Evaluate for malaria.
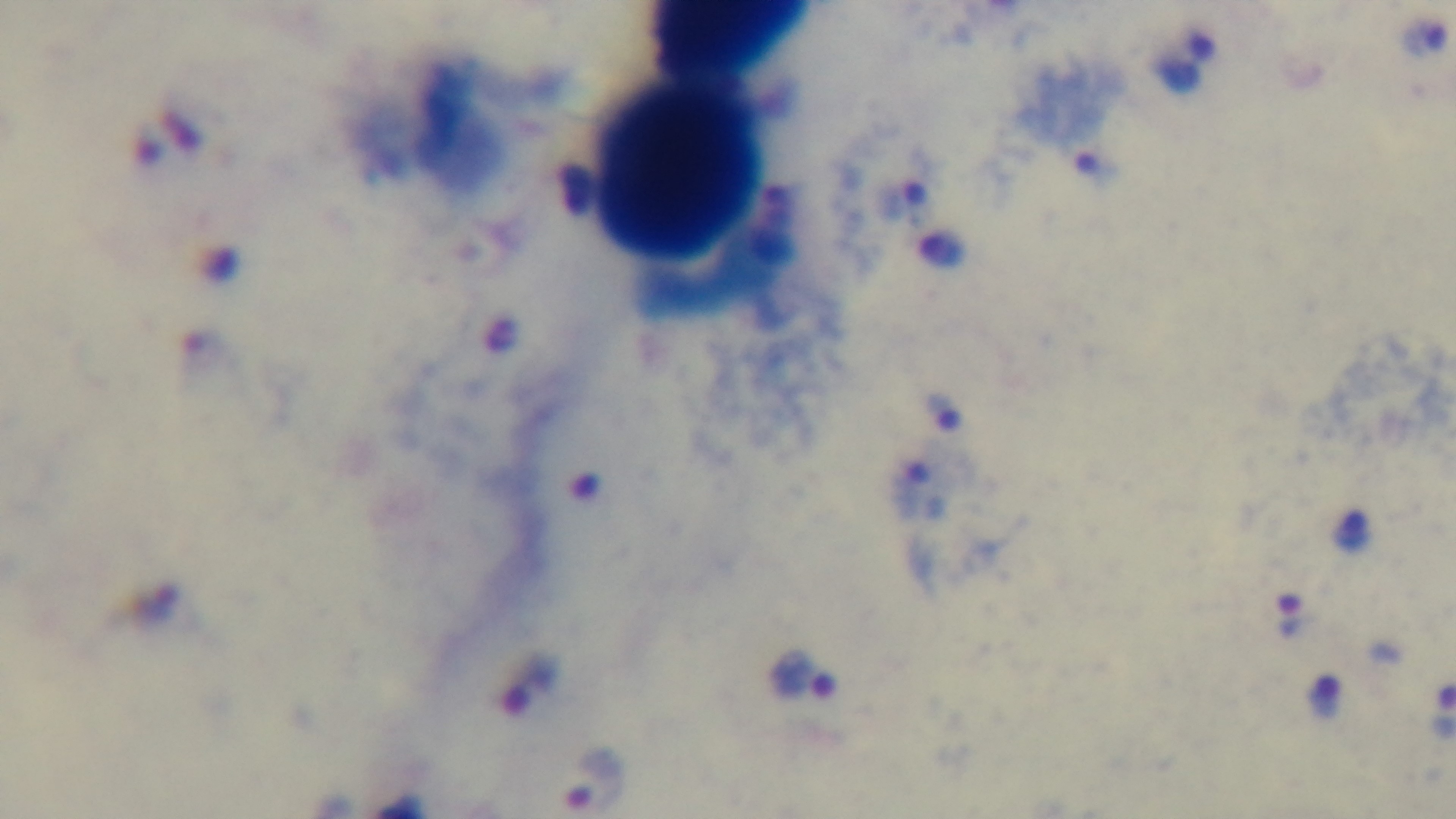

Infected.

Summary:
  - Objective: 100x oil immersion
  - Preparation: thick smear
  - Field of view: one from the slide
  - Stain: Giemsa
  - Capture: mounted 4K digital camera
  - Modality: light microscopy